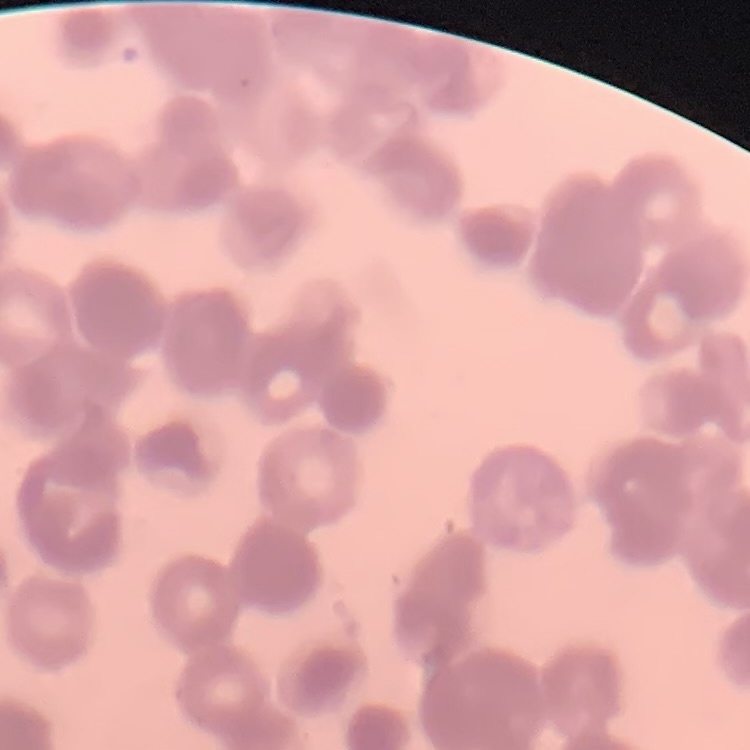
Summary:
  - Red blood cell morphology: rouleaux formation
  - Image type: one tile cut from a larger photomicrograph
  - Stain: Field's or Giemsa
  - Preparation: thin blood film